Outline each blood parasite and name the species.
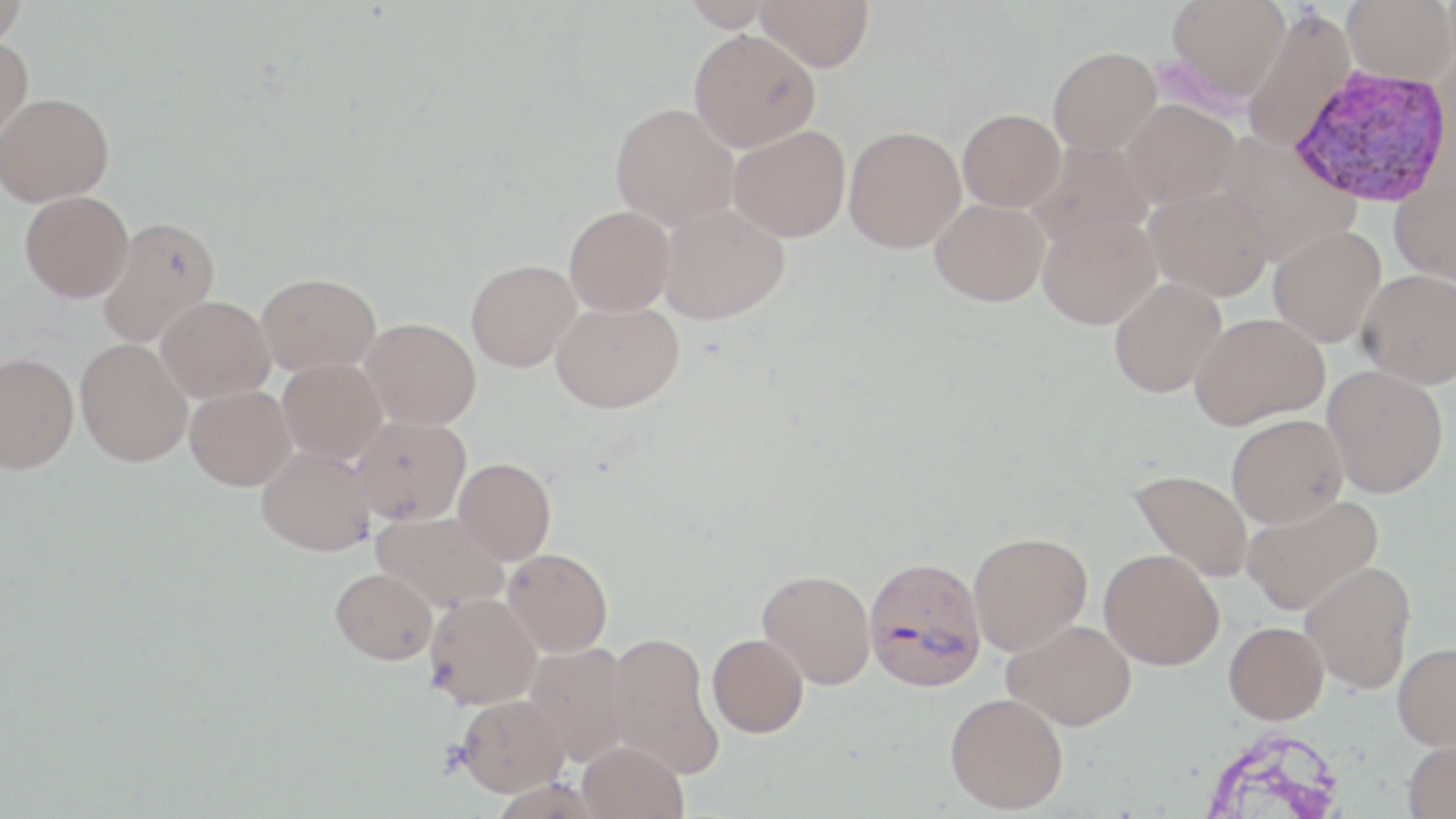
Approximate bounding boxes as (x1, y1, x2, y2) in pixels.
Plasmodium vivax-infected red blood cells: (1289, 64, 1453, 209), (863, 554, 987, 692).
No Plasmodium falciparum, Plasmodium ovale, Plasmodium malariae, Babesia divergens, or Trypanosoma brucei observed.

Summary:
  - Uninfected red blood cell locations: (0, 0, 27, 47), (679, 0, 777, 31), (754, 0, 874, 71), (1166, 0, 1290, 102), (1342, 0, 1456, 85), (1241, 8, 1355, 153), (689, 28, 821, 152), (0, 36, 33, 145), (1048, 46, 1161, 155), (0, 93, 114, 206), (1120, 99, 1241, 209), (611, 103, 739, 230), (958, 108, 1065, 211), (728, 125, 851, 242), (844, 126, 965, 253), (1213, 132, 1359, 264), (1028, 140, 1155, 249), (1389, 164, 1456, 287), (1145, 185, 1274, 301), (19, 190, 133, 302), (929, 198, 1050, 306), (658, 203, 789, 324), (564, 205, 675, 316), (1037, 212, 1161, 329), (97, 215, 220, 346), (1268, 226, 1386, 347), (466, 259, 581, 371), (1357, 269, 1456, 388), (256, 272, 380, 375), (1109, 278, 1226, 397), (156, 295, 275, 402), (551, 300, 683, 413), (1191, 312, 1329, 428), (361, 317, 481, 429), (75, 339, 192, 467), (0, 353, 79, 474), (278, 358, 387, 464), (1322, 365, 1448, 498), (185, 385, 296, 490), (1226, 414, 1347, 527), (352, 415, 470, 525), (257, 446, 376, 555), (453, 457, 556, 564), (1130, 469, 1254, 582), (1241, 493, 1384, 615), (372, 511, 509, 613), (968, 531, 1092, 655), (502, 547, 613, 657), (1099, 549, 1224, 669), (1299, 561, 1416, 694), (330, 568, 437, 664), (758, 570, 875, 689), (425, 593, 542, 709), (1003, 619, 1136, 731), (1224, 621, 1329, 724), (606, 632, 723, 777), (707, 634, 809, 737), (525, 643, 632, 766), (1393, 643, 1456, 749), (945, 692, 1068, 813), (457, 694, 569, 796), (1402, 736, 1456, 819), (578, 741, 688, 819)
  - Slide-level diagnosis: Plasmodium vivax
  - Magnification: 1000x
  - Preparation: thin blood smear
  - Field of view: single
  - Stain: May-Grünwald-Giemsa
  - Modality: light microscopy
  - Image size: 1456×819 pixels